Give the location of every WBC.
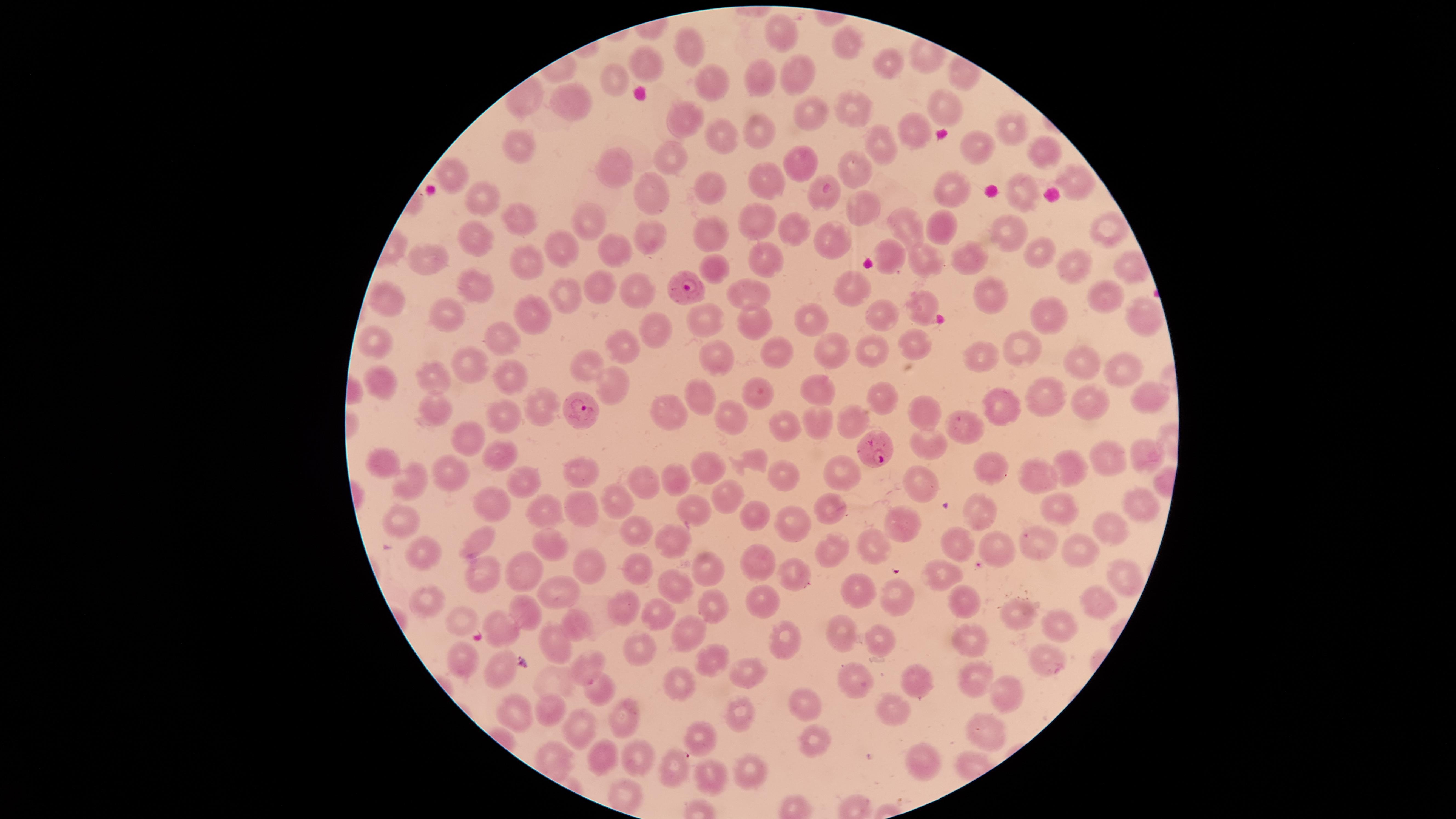
No WBCs identified.

{
  "visible_region": "circular",
  "parasitized_RBCs": "approximate marker points, in pixels from the top-left corner: (x=678, y=289), (x=585, y=403), (x=877, y=446)",
  "uninfected_RBCs": "approximate marker points, in pixels from the top-left corner: (x=781, y=34), (x=847, y=47), (x=688, y=48), (x=643, y=61), (x=888, y=66), (x=763, y=77), (x=800, y=77), (x=614, y=79), (x=707, y=85), (x=563, y=98), (x=946, y=105), (x=855, y=111), (x=809, y=113), (x=685, y=121), (x=1017, y=124), (x=908, y=127), (x=762, y=132), (x=726, y=140), (x=513, y=143), (x=881, y=145), (x=973, y=150), (x=1042, y=151), (x=669, y=159), (x=621, y=164), (x=797, y=165), (x=853, y=167), (x=453, y=172), (x=1077, y=178), (x=769, y=181), (x=710, y=191), (x=957, y=192), (x=1025, y=194), (x=655, y=195), (x=478, y=196), (x=856, y=205), (x=585, y=216), (x=510, y=217), (x=757, y=222), (x=940, y=225), (x=793, y=227), (x=909, y=228), (x=1101, y=231), (x=653, y=232), (x=714, y=234), (x=1010, y=234), (x=477, y=238), (x=831, y=245), (x=557, y=247), (x=621, y=249), (x=1034, y=250), (x=894, y=253), (x=768, y=255), (x=918, y=255), (x=431, y=256), (x=963, y=258), (x=534, y=263), (x=1076, y=265), (x=715, y=268), (x=607, y=287), (x=849, y=288), (x=473, y=289), (x=646, y=292), (x=739, y=293), (x=984, y=294), (x=570, y=296), (x=387, y=299), (x=1109, y=302), (x=925, y=303), (x=1138, y=308), (x=449, y=317), (x=526, y=318), (x=706, y=318), (x=884, y=318), (x=816, y=319), (x=1050, y=320), (x=752, y=324), (x=653, y=333), (x=372, y=340), (x=496, y=340), (x=621, y=340), (x=918, y=344), (x=1022, y=347), (x=829, y=350), (x=873, y=351), (x=772, y=352), (x=715, y=354), (x=978, y=356), (x=473, y=361), (x=1077, y=361), (x=592, y=365), (x=1120, y=368), (x=515, y=372), (x=434, y=375), (x=614, y=378), (x=381, y=382), (x=759, y=388), (x=819, y=391), (x=698, y=396), (x=1146, y=396), (x=1042, y=398), (x=882, y=400), (x=1095, y=402), (x=539, y=406), (x=1005, y=409), (x=922, y=410), (x=505, y=411), (x=671, y=411), (x=437, y=412), (x=728, y=416), (x=851, y=422), (x=819, y=424), (x=781, y=425), (x=953, y=428), (x=471, y=431), (x=929, y=439), (x=493, y=447), (x=1144, y=452), (x=758, y=453), (x=1105, y=455), (x=386, y=458), (x=987, y=461), (x=1079, y=467), (x=707, y=469), (x=590, y=471), (x=840, y=473), (x=454, y=475), (x=527, y=476), (x=1037, y=476), (x=782, y=477), (x=409, y=478), (x=677, y=478), (x=922, y=480), (x=646, y=481), (x=724, y=492), (x=1142, y=498), (x=498, y=499), (x=1053, y=501), (x=693, y=504), (x=617, y=505), (x=577, y=507), (x=829, y=508), (x=982, y=510), (x=539, y=511), (x=754, y=512), (x=403, y=520), (x=897, y=521), (x=790, y=523), (x=1110, y=531), (x=636, y=532), (x=479, y=540), (x=667, y=540), (x=1036, y=541), (x=552, y=545), (x=833, y=545), (x=871, y=547), (x=957, y=547), (x=1085, y=547), (x=993, y=549), (x=423, y=553), (x=763, y=560), (x=596, y=565), (x=528, y=567), (x=640, y=571), (x=707, y=571), (x=1130, y=574), (x=483, y=575), (x=945, y=576), (x=792, y=579), (x=672, y=580), (x=562, y=588), (x=857, y=592), (x=896, y=596), (x=427, y=598), (x=765, y=600), (x=961, y=601), (x=710, y=603), (x=1094, y=604), (x=629, y=609), (x=661, y=613), (x=533, y=614), (x=1017, y=616), (x=458, y=619), (x=1058, y=624), (x=578, y=625), (x=508, y=633), (x=684, y=633), (x=846, y=633), (x=787, y=638), (x=886, y=639), (x=972, y=640), (x=557, y=646), (x=646, y=651), (x=716, y=657), (x=468, y=659), (x=1046, y=661), (x=590, y=666), (x=503, y=670), (x=749, y=673), (x=913, y=678), (x=854, y=680), (x=975, y=680), (x=684, y=689), (x=1004, y=690), (x=600, y=692), (x=799, y=695), (x=887, y=706), (x=631, y=708), (x=550, y=710), (x=517, y=711), (x=738, y=712), (x=586, y=725), (x=984, y=729), (x=815, y=738), (x=707, y=740), (x=606, y=756), (x=638, y=761), (x=918, y=764), (x=673, y=765), (x=715, y=770), (x=743, y=770), (x=620, y=791)",
  "preparation": "thin smear of blood",
  "field_of_view": "single",
  "presence": "malaria parasites seen",
  "stain": "Giemsa",
  "species": "Plasmodium falciparum",
  "capture": "smartphone photograph through the microscope eyepiece",
  "image_size": "1456×819 pixels"
}